Report the malaria status of this cell.
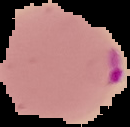

It is parasitized.

Summary:
  - Preparation: thin blood smear
  - Image type: segmented cell region on a black background
  - Image size: 130×127 pixels